Outline each P. falciparum parasite and classify it by life-cycle stage.
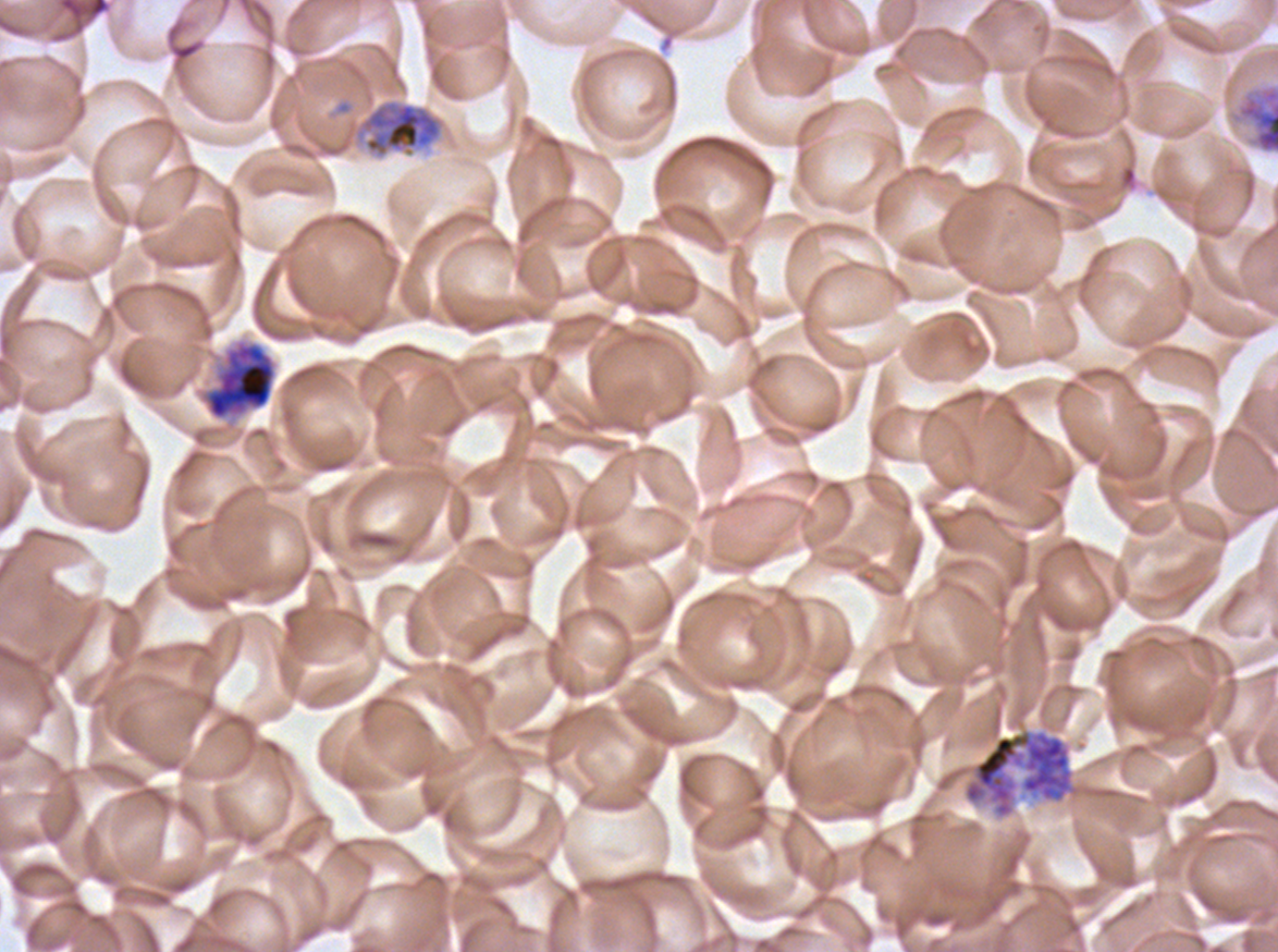
Approximate bounding boxes as (x1, y1, x2, y2) in pixels.
Early schizonts: (1232, 83, 1277, 154), (353, 99, 444, 159), (197, 337, 278, 424).
Late schizonts: (964, 729, 1074, 818).
No rings, late-ring/early-trophozoite forms, mid trophozoites, late trophozoites, segmenters, or gametocytes observed.

image_size: 1278×952 pixels
life_cycle_stages_observed: early schizont, late schizont
specimen: ex-vivo P. falciparum culture from a patient in The Gambia, grown for 24 to 48 hours
preparation: thin blood smear
stain: Giemsa
field_of_view: sub-image separated from a larger composite